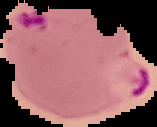
Summary:
  - Malaria status: parasitized
  - Preparation: thin blood smear
  - Image size: 157×127 pixels
  - Image type: cell region segmented out of the field of view; surrounding area masked to black